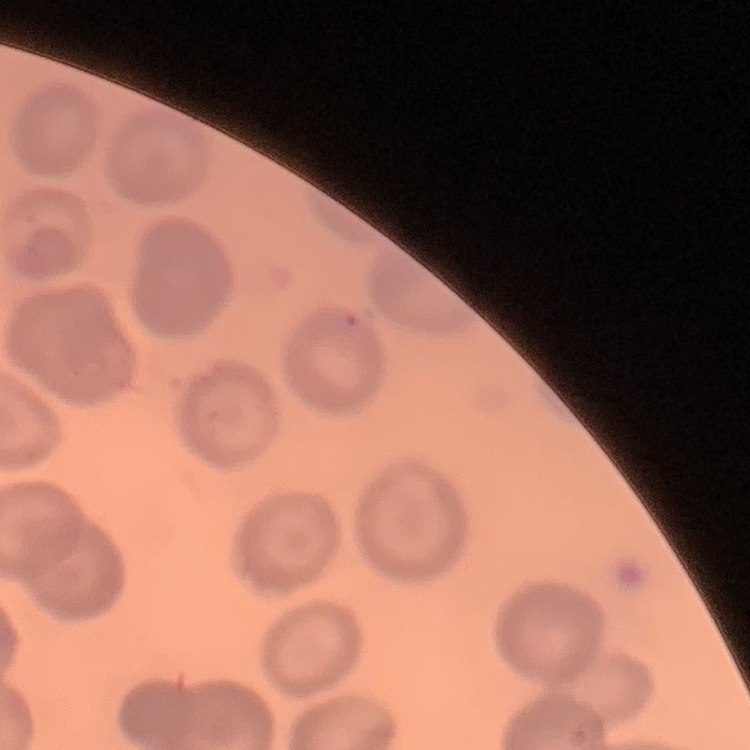

red blood cell morphology = no rouleaux formation
preparation = thin peripheral smear
stain = Field's or Giemsa
image type = one tile cut from a larger photomicrograph